Assess this cell for malaria.
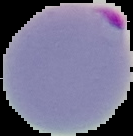
It is parasitized.

image size = 133×136 pixels
image type = segmented cell region on a black background
preparation = thin blood film